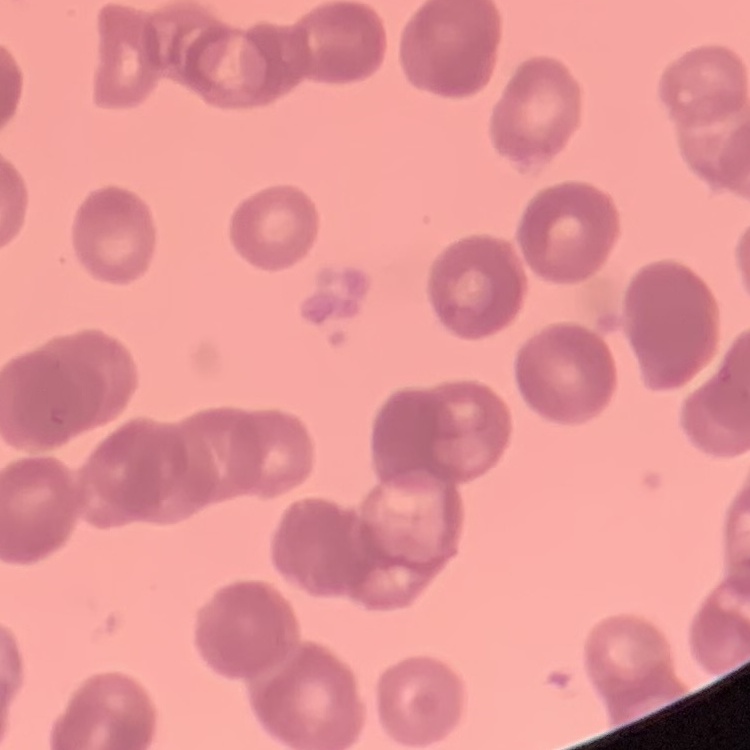
Summary:
  - Erythrocyte morphology: rouleaux formation
  - Preparation: thin peripheral smear
  - Stain: Field's or Giemsa
  - Image type: one tile cut from a larger photomicrograph